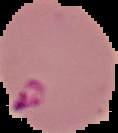
image size = 118×133 pixels
image type = segmented cell region with the area outside set to black
preparation = thin blood film
result = Plasmodium parasites detected